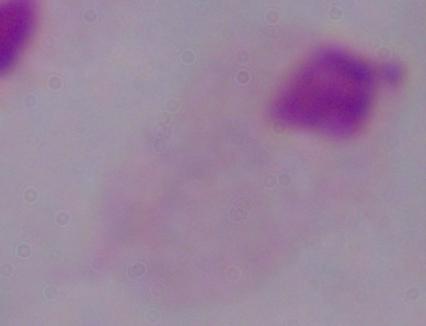

1000x magnification. Micrograph. A trichomonad is seen.